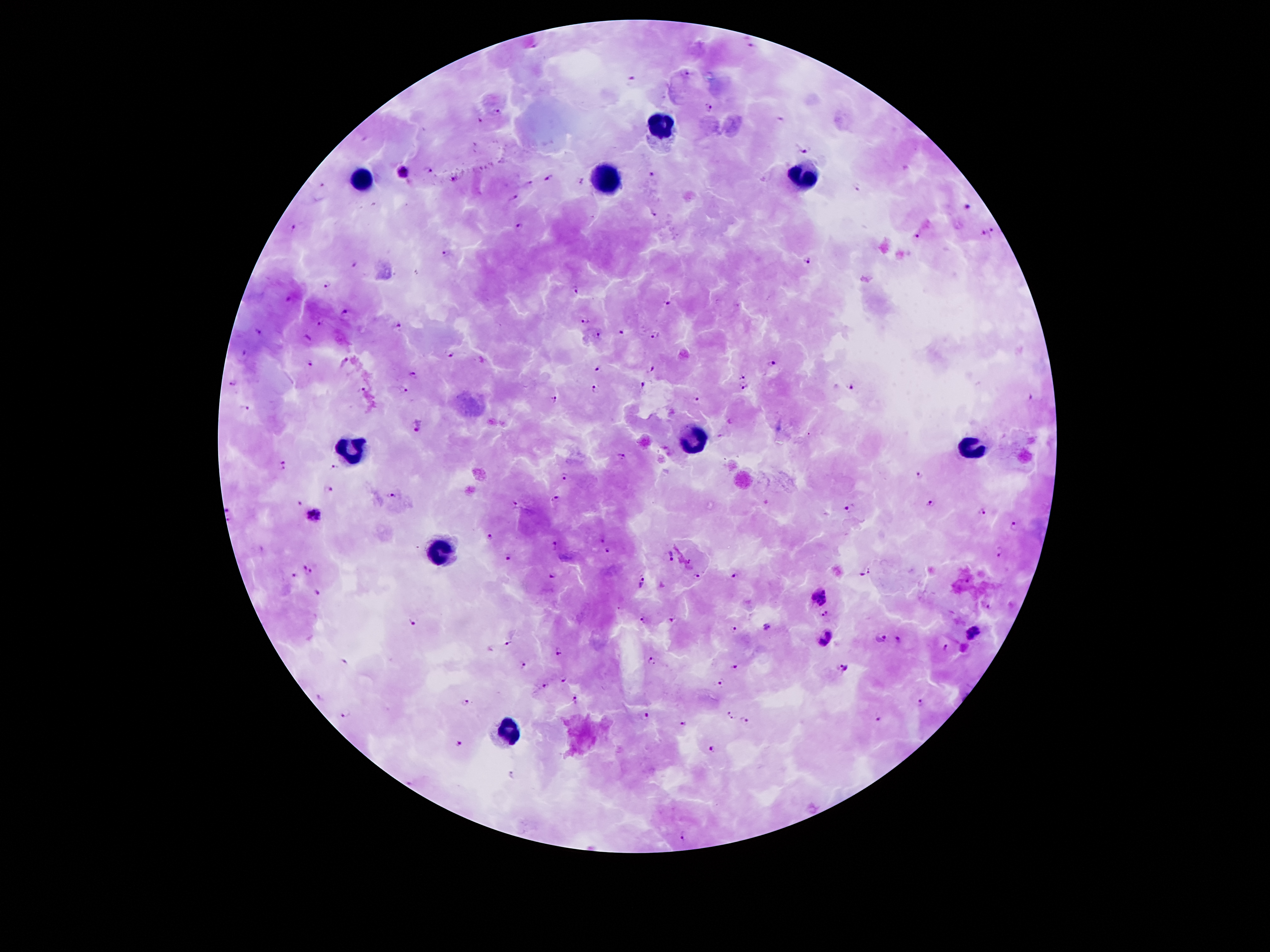
coordinate format = approximate object centers, in pixels from the top-left corner
leukocyte locations = (x=663, y=127), (x=802, y=176), (x=363, y=181), (x=605, y=181), (x=699, y=440), (x=351, y=445), (x=972, y=446), (x=445, y=549), (x=508, y=732)
Plasmodium parasite locations = (x=533, y=46), (x=753, y=46), (x=689, y=74), (x=631, y=79), (x=707, y=109), (x=497, y=111), (x=480, y=119), (x=781, y=119), (x=804, y=149), (x=430, y=168), (x=405, y=173), (x=649, y=175), (x=551, y=177), (x=453, y=180), (x=581, y=180), (x=528, y=182), (x=320, y=186), (x=857, y=187), (x=513, y=198), (x=967, y=206), (x=653, y=215), (x=294, y=225), (x=520, y=225), (x=994, y=229), (x=919, y=234), (x=984, y=236), (x=447, y=252), (x=808, y=261), (x=353, y=264), (x=327, y=283), (x=575, y=290), (x=289, y=298), (x=667, y=304), (x=344, y=309), (x=320, y=321), (x=585, y=322), (x=399, y=327), (x=258, y=330), (x=620, y=332), (x=653, y=334), (x=597, y=336), (x=307, y=337), (x=244, y=354), (x=451, y=354), (x=345, y=361), (x=311, y=362), (x=772, y=366), (x=596, y=369), (x=650, y=369), (x=742, y=375), (x=413, y=376), (x=232, y=384), (x=642, y=384), (x=849, y=386), (x=361, y=387), (x=743, y=387), (x=594, y=388), (x=403, y=389), (x=1028, y=396), (x=696, y=399), (x=555, y=400), (x=247, y=406), (x=730, y=420), (x=418, y=425), (x=719, y=436), (x=666, y=446), (x=620, y=458), (x=284, y=463), (x=334, y=468), (x=919, y=474), (x=564, y=478), (x=329, y=487), (x=392, y=494), (x=557, y=498), (x=764, y=502), (x=515, y=503), (x=931, y=503), (x=300, y=504), (x=228, y=510), (x=849, y=510), (x=983, y=510), (x=313, y=514), (x=1014, y=525), (x=490, y=537), (x=603, y=540), (x=555, y=545), (x=260, y=547), (x=609, y=550), (x=998, y=550), (x=672, y=553), (x=509, y=556), (x=306, y=570), (x=865, y=572), (x=553, y=575), (x=734, y=575), (x=292, y=576), (x=699, y=576), (x=966, y=578), (x=641, y=583), (x=317, y=594), (x=821, y=597), (x=987, y=604), (x=825, y=614), (x=644, y=618), (x=673, y=619), (x=413, y=623), (x=765, y=626), (x=732, y=628), (x=975, y=633), (x=830, y=634), (x=881, y=636), (x=898, y=638), (x=509, y=642), (x=823, y=645), (x=945, y=647), (x=559, y=651), (x=652, y=659), (x=345, y=661), (x=522, y=663), (x=735, y=665), (x=841, y=669), (x=563, y=680), (x=719, y=683), (x=546, y=684), (x=319, y=695), (x=575, y=700), (x=466, y=702), (x=919, y=703), (x=346, y=714), (x=643, y=715), (x=731, y=717), (x=880, y=720), (x=746, y=722), (x=682, y=724), (x=458, y=745), (x=713, y=748), (x=513, y=776), (x=681, y=837)
capture = smartphone camera through the microscope eyepiece
stain = Giemsa
preparation = thick peripheral-blood smear
magnification = 100x
image size = 1270×952 pixels
patient malaria status = infected with Plasmodium falciparum
field of view = single